Locate every Plasmodium parasite by life-cycle stage, and every leukocyte.
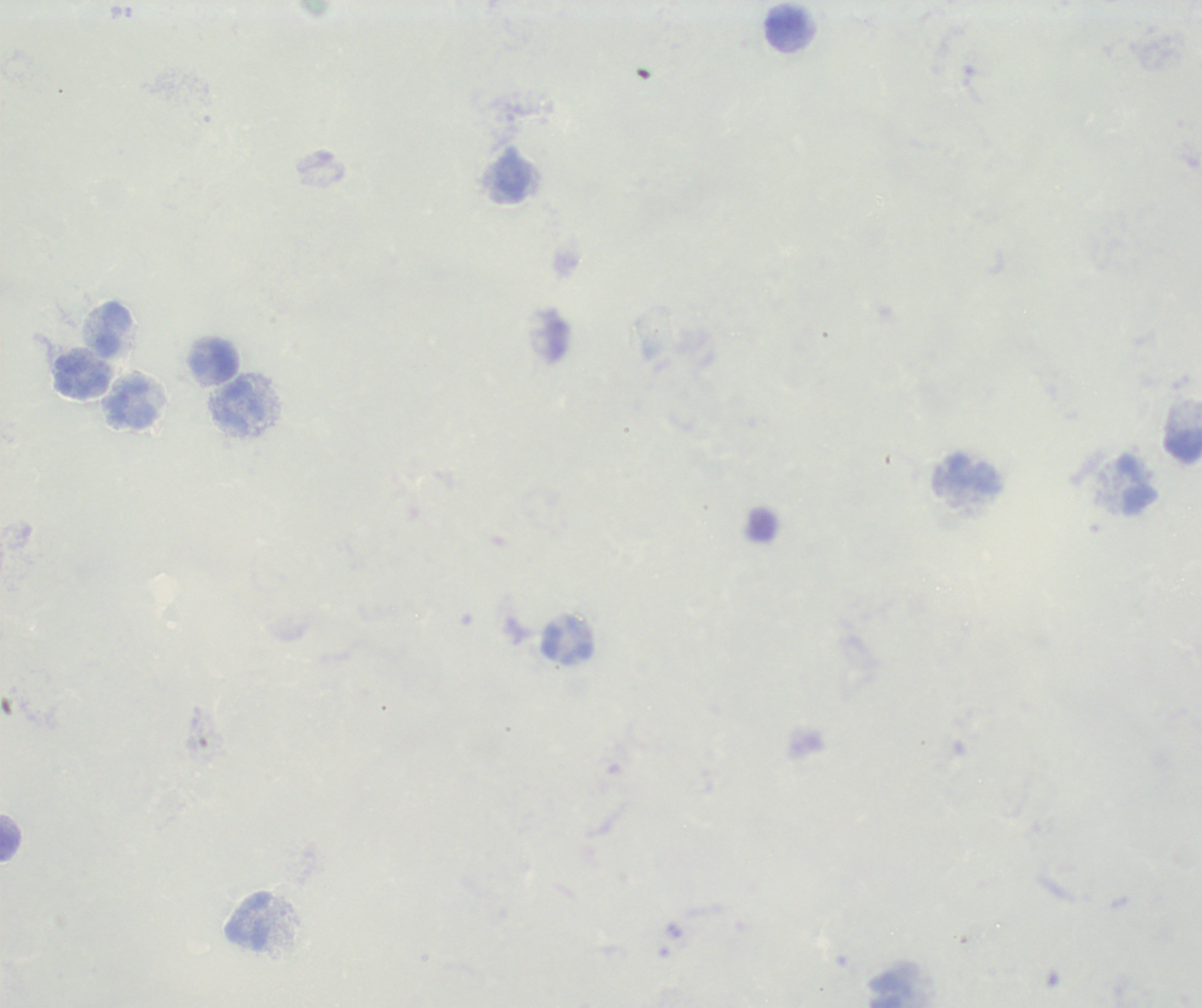
No Plasmodium parasites detected.
Approximate centers as {x, y} in pixels.
Leukocytes: {787, 27}, {513, 177}, {113, 328}, {216, 360}, {83, 374}, {133, 404}, {241, 405}, {1184, 444}, {973, 476}, {1137, 484}, {568, 642}, {10, 837}, {249, 921}, {887, 990}.

stain = Romanowsky
context = previously used in an actual diagnosis
preparation = thick smear of blood
background quality = poor
magnification = 100x
image size = 1202×1008 pixels
field of view = single